Name the blood parasite species.
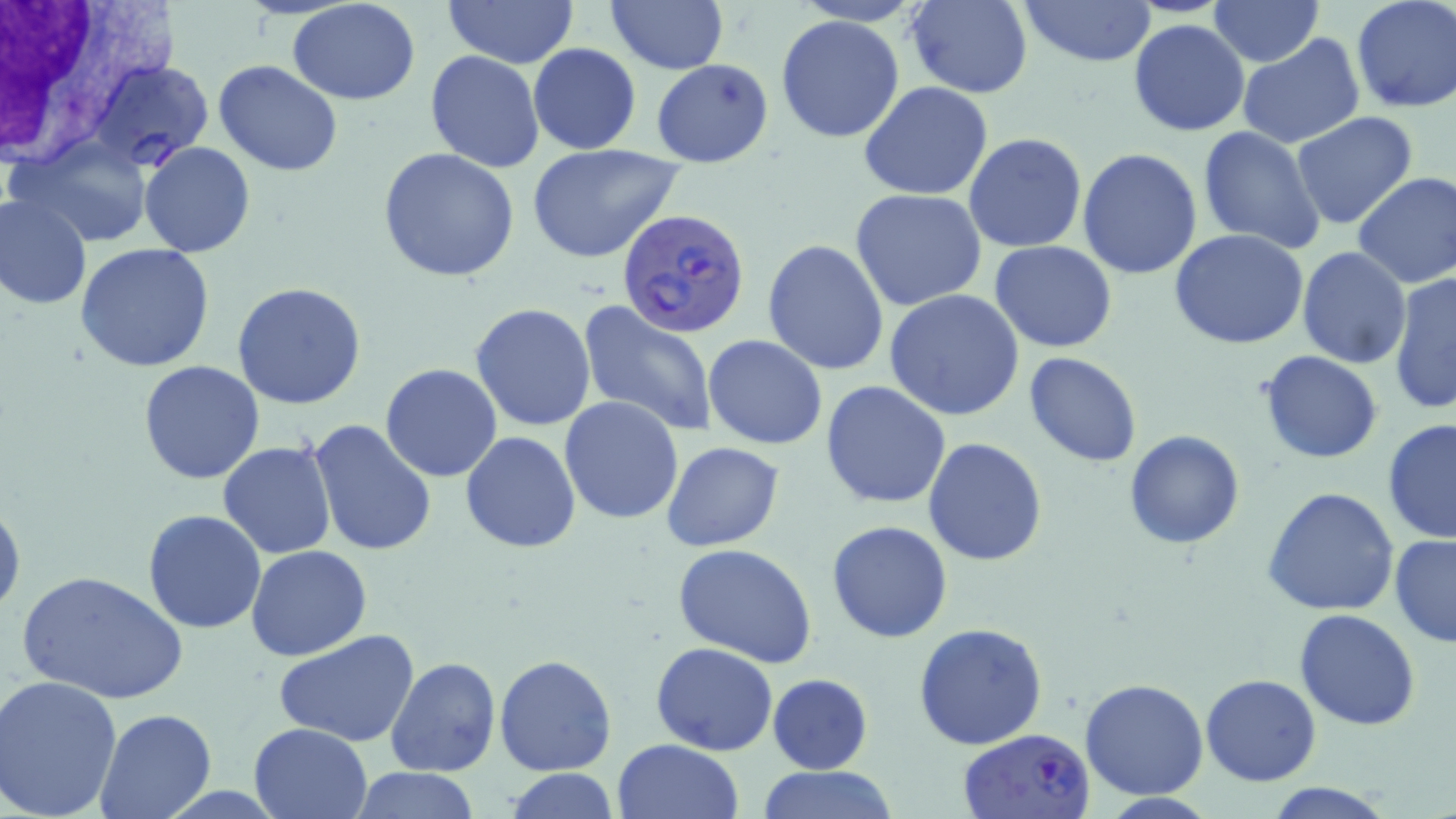

Plasmodium falciparum.

Summary:
  - Coordinate format: approximate bounding boxes as (x1,y1)-(x2,y2) corner pairs in pixels
  - Plasmodium falciparum-infected red blood cell locations: (618,211)-(753,343), (957,727)-(1096,819)
  - White blood cell locations: (0,1)-(184,167)
  - Uninfected red blood cell locations: (286,0)-(421,105), (441,0)-(580,67), (904,0)-(1033,98), (1016,0)-(1157,69), (1350,0)-(1456,115), (605,1)-(729,75), (1211,2)-(1323,65), (775,14)-(905,144), (1128,20)-(1251,137), (1239,33)-(1365,148), (528,42)-(641,155), (425,50)-(544,173), (86,59)-(212,171), (650,59)-(774,168), (214,61)-(342,177), (860,82)-(993,200), (1292,111)-(1419,229), (1195,126)-(1327,254), (964,133)-(1088,254), (12,137)-(155,249), (139,141)-(255,257), (525,143)-(685,264), (379,148)-(519,284), (1078,149)-(1204,280), (1353,171)-(1456,289), (849,190)-(988,312), (0,194)-(94,310), (1169,230)-(1311,350), (762,239)-(889,376), (989,240)-(1117,352), (75,242)-(218,374), (1297,246)-(1412,368), (1389,272)-(1455,416), (232,281)-(367,410), (884,289)-(1026,420), (575,300)-(720,436), (470,303)-(597,432), (703,334)-(827,450), (1259,349)-(1383,463), (1023,351)-(1143,468), (139,360)-(266,485), (380,364)-(502,483), (821,381)-(951,509), (559,396)-(685,525), (1382,416)-(1456,548), (308,419)-(438,559), (1124,429)-(1246,548), (461,430)-(582,553), (922,437)-(1048,566), (218,441)-(337,559), (662,442)-(785,550), (1264,485)-(1399,616), (0,493)-(24,622), (142,510)-(266,632), (828,521)-(951,643), (1389,533)-(1456,649), (672,543)-(818,668), (246,546)-(372,662), (17,568)-(188,704), (1295,609)-(1422,731), (914,622)-(1048,751), (273,630)-(420,747), (650,642)-(777,755), (494,654)-(617,775), (386,656)-(501,776), (767,673)-(872,775), (1201,674)-(1322,786), (1,675)-(122,819), (1080,678)-(1208,800), (95,706)-(216,819), (249,722)-(371,818), (613,739)-(743,819), (350,766)-(482,819), (752,767)-(901,819), (503,770)-(624,818), (1263,780)-(1398,818)
  - Modality: optical microscopy
  - Preparation: thin blood smear
  - Field of view: one of a larger specimen
  - Stain: May-Grünwald-Giemsa
  - Image size: 1456×819 pixels
  - Magnification: 1000x